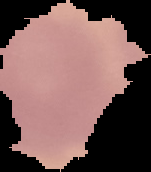

malaria status = uninfected
image size = 151×172 pixels
image type = segmented cell region with the area outside set to black
preparation = thin blood smear